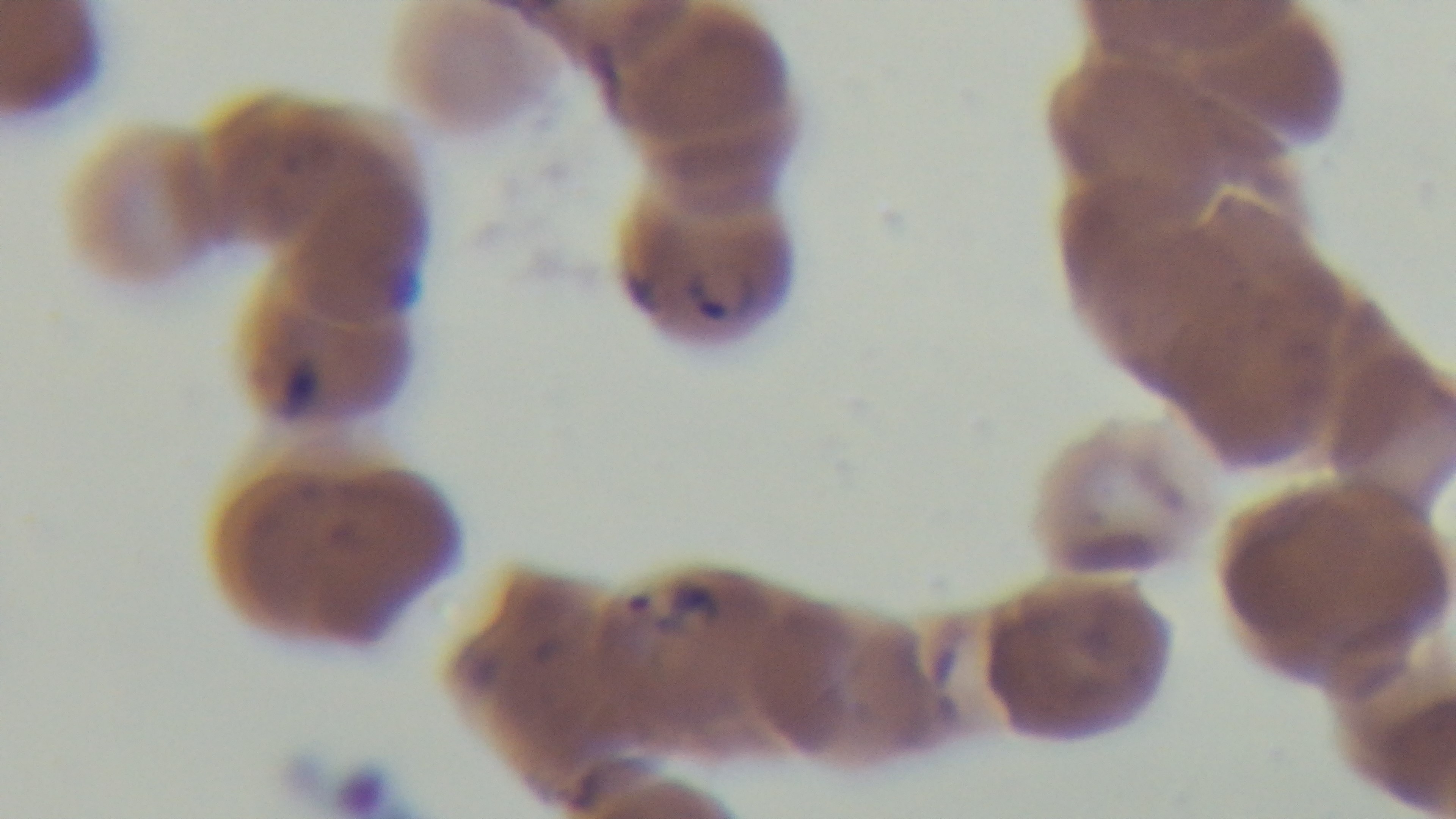

stain = Giemsa
objective = 100x oil immersion
field of view = single
preparation = thin smear
malaria status = positive
modality = light microscopy
capture = mounted 4K digital camera